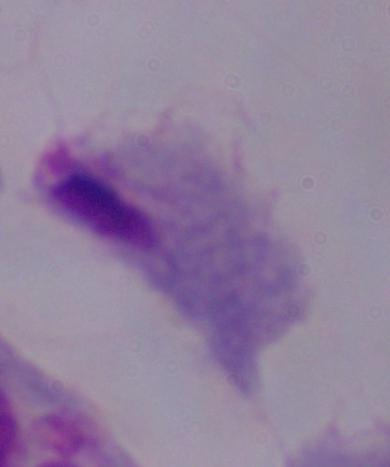

Micrograph. 1000x magnification. A trichomonad is shown.